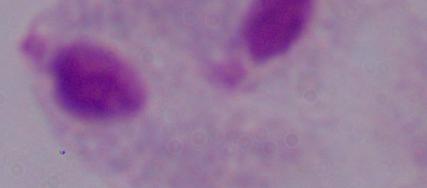
A trichomonad is shown. Captured at 1000x magnification. Photomicrograph.